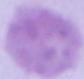
identification = red blood cell
magnification = 1000x
modality = photomicrograph